Classify the preparation.
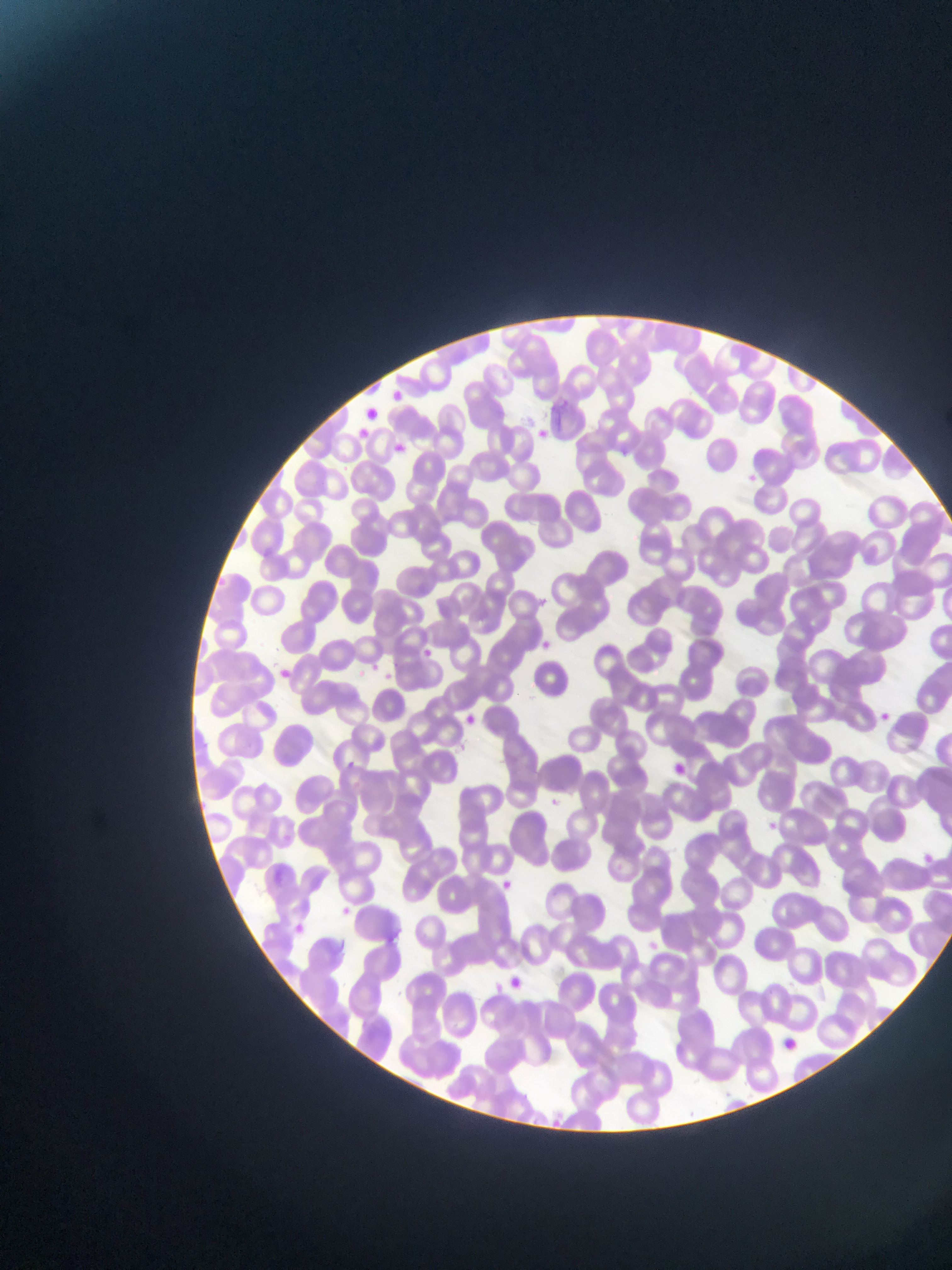
This is a thin smear.

capture = mobile-phone photograph through a microscope
malaria parasite locations = approximate bounding boxes as (left, top, right, bottom) in pixels: (389, 389, 405, 401), (552, 400, 572, 410), (532, 426, 561, 444), (389, 439, 407, 458), (615, 445, 633, 455), (744, 473, 761, 484), (536, 592, 545, 603), (540, 640, 557, 652), (424, 643, 435, 663), (369, 659, 385, 672), (275, 663, 303, 686), (383, 667, 395, 684), (875, 709, 895, 721), (463, 711, 475, 728), (341, 758, 361, 774), (552, 795, 570, 806), (764, 815, 781, 837), (920, 851, 935, 866), (501, 875, 526, 891), (336, 907, 354, 919), (293, 920, 309, 933), (644, 936, 663, 955)
image size = 952×1270 pixels
country = Ghana
field of view = single